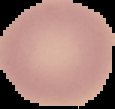

image_size: 115×109 pixels
preparation: thin blood film
image_type: cell region segmented out of the field of view; surrounding area masked to black
malaria_status: uninfected